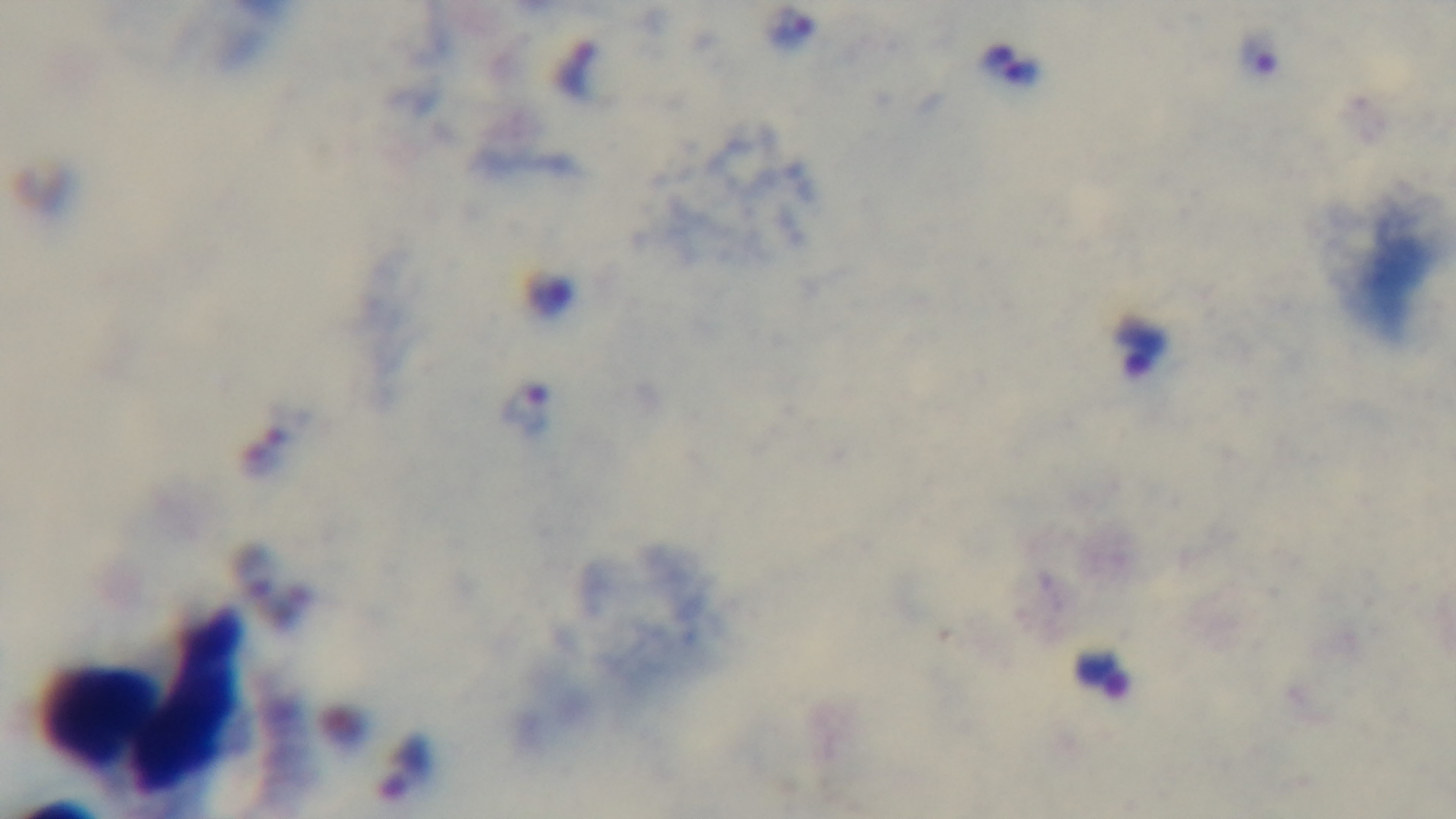
Summary:
  - Capture: mounted 4K digital camera
  - Field of view: one from the slide
  - Preparation: thick smear
  - Stain: Giemsa
  - Objective: 100x oil immersion
  - Modality: light microscopy
  - Malaria status: positive